Assess the morphology of the red blood cells.
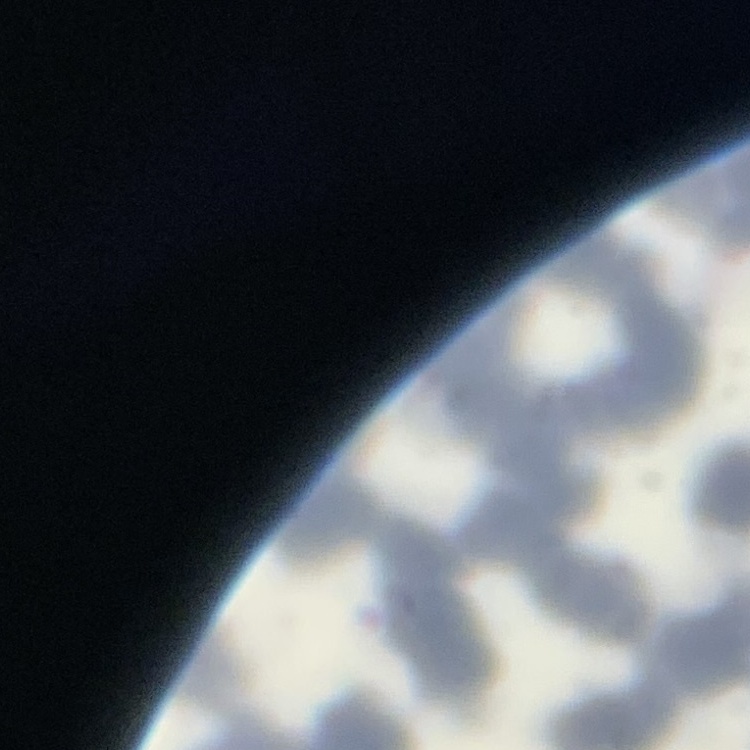
Rouleaux formation.

Summary:
  - Image type: one tile cut from a larger photomicrograph
  - Preparation: thin blood film
  - Stain: Field's or Giemsa